Report the malaria status of this cell.
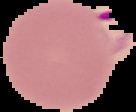
It is parasitized.

{
  "image_type": "segmented cell region on a black background",
  "image_size": "136×112 pixels",
  "preparation": "thin blood film"
}